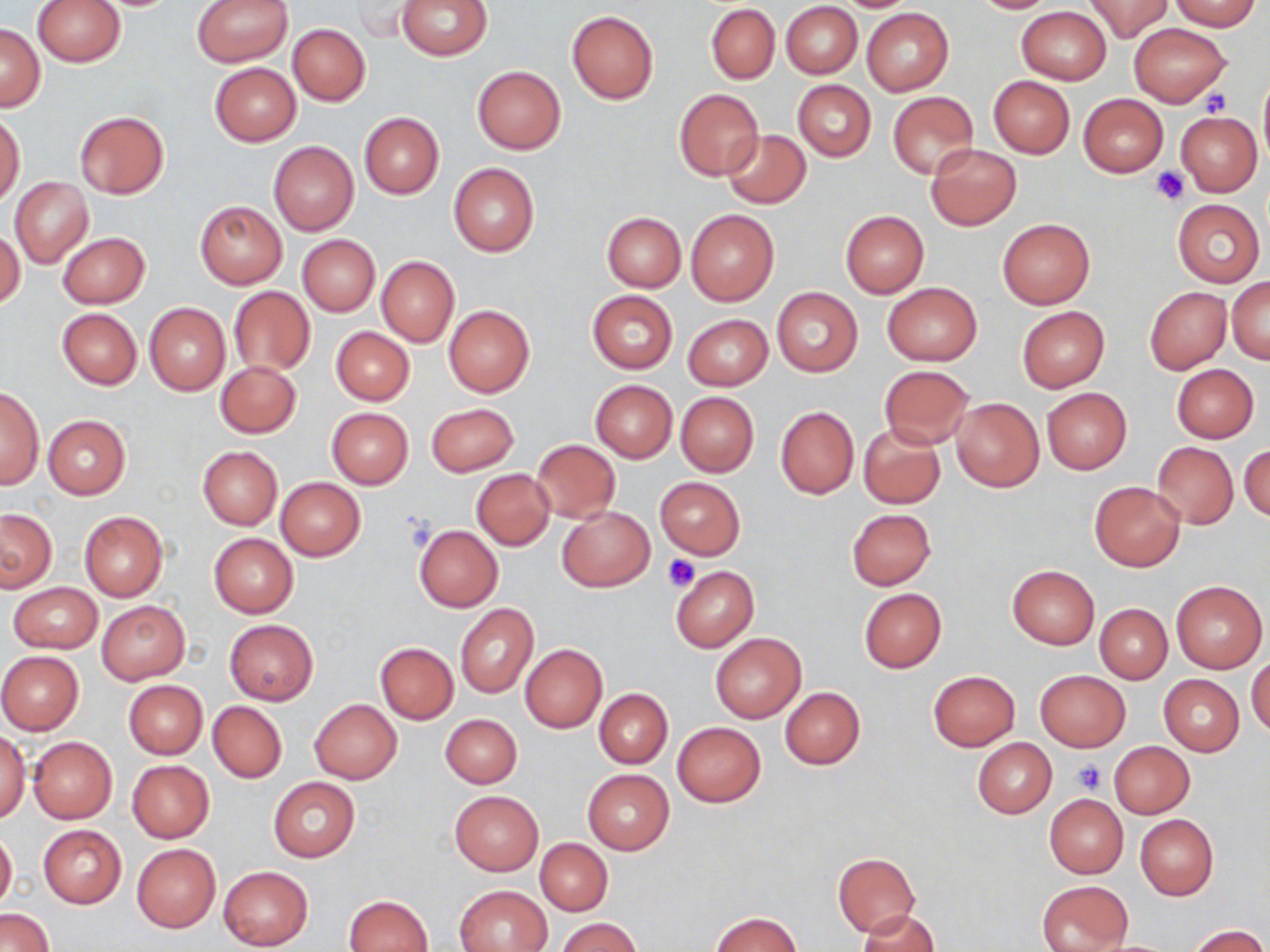

Summary:
  - Coordinate format: approximate bounding boxes as (x1, y1, x2, y2) in pixels
  - Platelet locations: (1200, 88, 1232, 117), (1152, 167, 1190, 205), (662, 554, 701, 592), (1074, 761, 1107, 793)
  - Uninfected red blood cell locations: (32, 0, 126, 67), (191, 0, 293, 67), (395, 0, 492, 59), (967, 0, 1059, 14), (1084, 0, 1174, 42), (1168, 1, 1262, 31), (781, 2, 862, 78), (348, 3, 425, 41), (705, 4, 779, 84), (1017, 6, 1111, 84), (861, 8, 954, 96), (567, 10, 658, 104), (1130, 22, 1231, 106), (288, 23, 370, 105), (0, 25, 44, 110), (210, 62, 300, 146), (472, 66, 566, 155), (1259, 68, 1270, 169), (988, 76, 1075, 158), (792, 81, 875, 161), (673, 88, 763, 180), (888, 92, 977, 180), (1078, 93, 1168, 176), (0, 111, 25, 205), (73, 111, 169, 198), (1176, 111, 1262, 196), (359, 113, 444, 198), (721, 130, 811, 209), (268, 141, 358, 236), (926, 144, 1022, 230), (449, 163, 539, 257), (10, 177, 93, 267), (1172, 199, 1264, 287), (195, 200, 287, 289), (685, 209, 778, 306), (839, 210, 930, 298), (602, 212, 685, 291), (997, 219, 1094, 309), (1, 228, 24, 307), (58, 232, 150, 309), (296, 234, 379, 317), (377, 257, 459, 347), (1228, 277, 1270, 364), (881, 282, 982, 365), (229, 287, 315, 377), (1145, 287, 1231, 373), (772, 288, 863, 377), (588, 290, 677, 373), (144, 303, 230, 396), (443, 305, 534, 396), (1017, 307, 1109, 391), (57, 308, 141, 389), (683, 314, 773, 391), (331, 326, 414, 405), (215, 361, 301, 438), (1170, 363, 1259, 443), (877, 365, 975, 449), (590, 380, 677, 463), (1, 386, 44, 491), (1042, 388, 1132, 474), (675, 392, 758, 476), (951, 398, 1043, 490), (426, 402, 519, 475), (774, 406, 859, 498), (326, 407, 413, 487), (44, 415, 130, 499), (858, 424, 945, 509), (532, 441, 620, 522), (1153, 442, 1238, 529), (1240, 443, 1269, 523), (197, 446, 282, 529), (472, 469, 554, 549), (655, 477, 745, 560), (276, 478, 365, 561), (1089, 481, 1186, 572), (556, 505, 655, 592), (846, 508, 936, 591), (1, 509, 56, 592), (80, 511, 167, 600), (414, 525, 502, 611), (208, 533, 298, 618), (671, 565, 758, 651), (1007, 565, 1099, 649), (1171, 581, 1267, 673), (9, 583, 103, 653), (859, 588, 946, 672), (96, 600, 190, 685), (1094, 603, 1172, 683), (455, 604, 537, 698), (225, 619, 319, 705), (711, 632, 806, 723), (376, 642, 458, 724), (521, 644, 607, 732), (0, 652, 83, 734), (1247, 655, 1270, 738), (1035, 669, 1130, 752), (928, 670, 1020, 750), (1160, 675, 1244, 756), (123, 680, 207, 759), (780, 687, 864, 768), (593, 688, 672, 768), (310, 699, 402, 783), (208, 702, 287, 783), (440, 713, 521, 788), (673, 721, 765, 807), (0, 731, 30, 820), (28, 736, 117, 823), (971, 737, 1056, 818), (1109, 741, 1194, 818), (127, 760, 214, 842), (583, 770, 673, 854), (268, 777, 361, 862), (449, 790, 543, 875), (1044, 794, 1128, 878), (1135, 815, 1218, 899), (38, 825, 126, 908), (0, 828, 17, 914), (535, 838, 613, 915), (132, 844, 220, 931), (833, 852, 920, 937), (218, 866, 313, 950), (1037, 881, 1131, 951), (454, 884, 553, 951), (344, 894, 433, 952), (0, 908, 54, 951), (859, 909, 940, 952), (711, 912, 802, 951), (558, 918, 641, 952), (1186, 926, 1266, 952)
  - Slide-level diagnosis: no evidence of blood parasites
  - Stain: May-Grünwald-Giemsa
  - Magnification: 1000x
  - Modality: light microscopy
  - Image size: 1270×952 pixels
  - Field of view: one of a larger specimen
  - Preparation: thin blood film